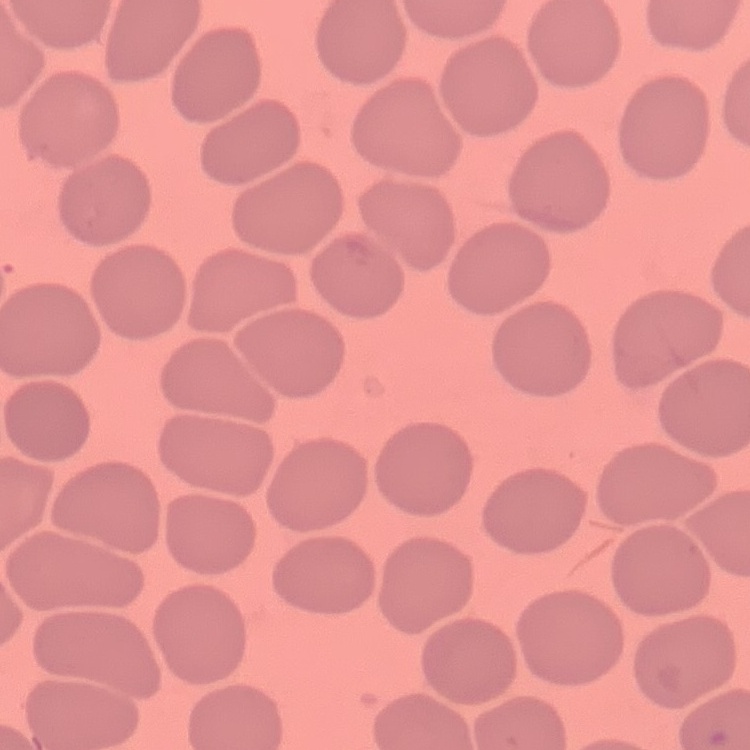
erythrocyte morphology = no rouleaux formation
image type = square crop of a larger photomicrograph
stain = Field's or Giemsa
preparation = thin blood smear